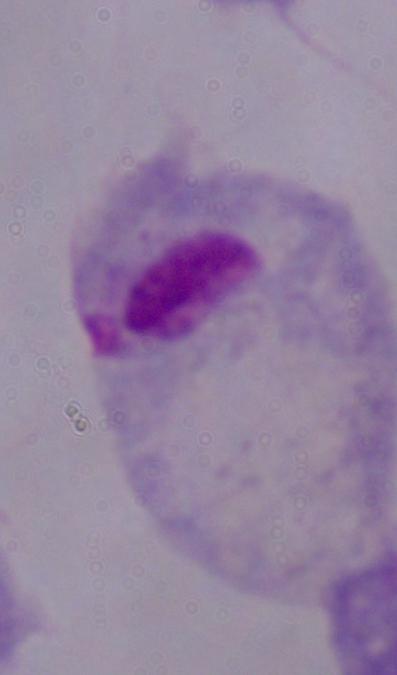

identification = trichomonad
modality = micrograph
magnification = 1000x